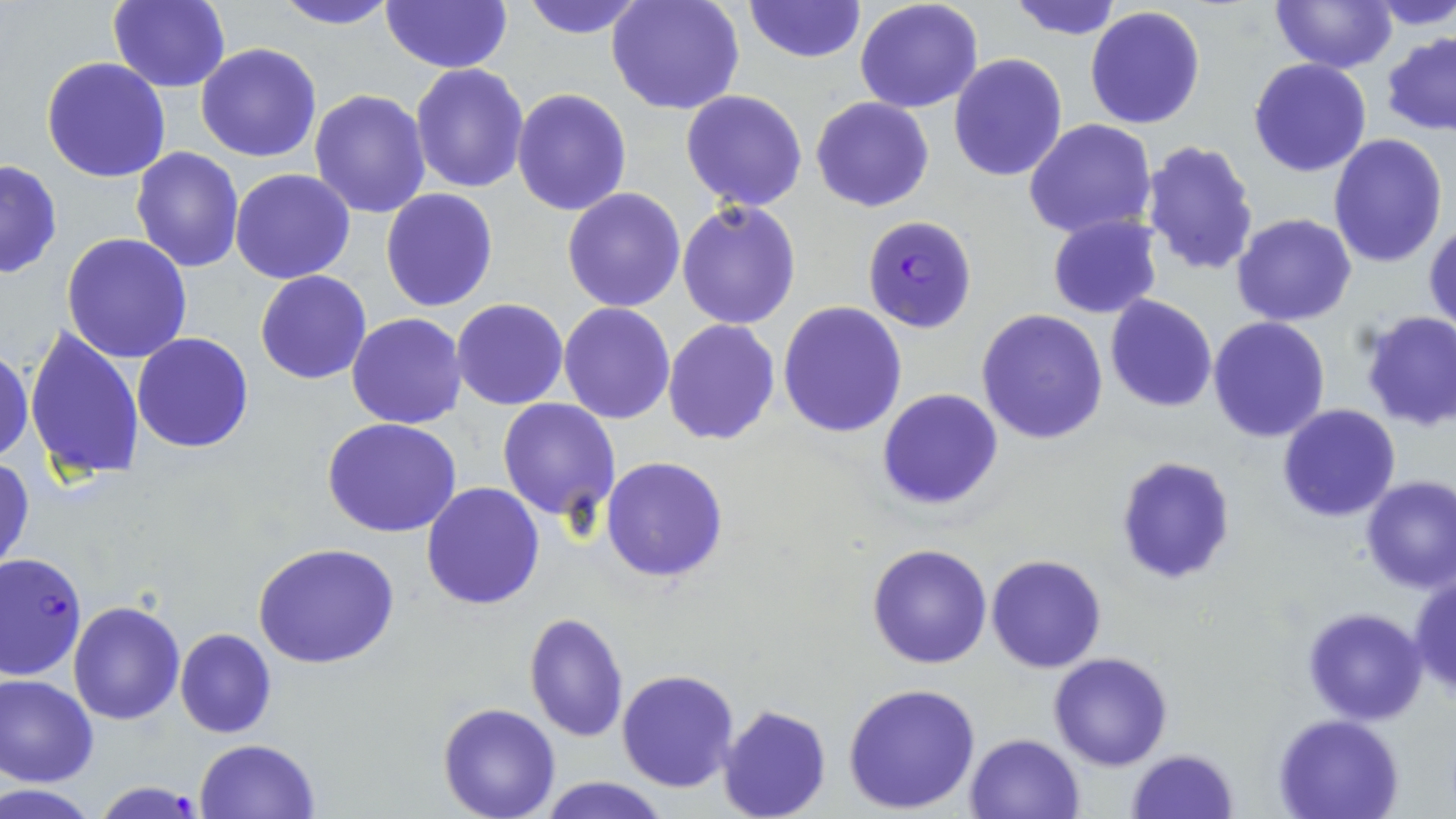

Summary:
  - Coordinate format: approximate bounding boxes as (x1, y1, x2, y2) in pixels
  - Plasmodium falciparum-infected red blood cell locations: (862, 214, 977, 332), (0, 552, 87, 683), (90, 779, 208, 818)
  - Uninfected red blood cell locations: (108, 0, 230, 93), (268, 0, 402, 30), (520, 0, 648, 39), (606, 0, 746, 117), (744, 0, 865, 64), (1005, 0, 1125, 41), (1269, 0, 1397, 72), (1370, 0, 1456, 30), (381, 1, 512, 74), (854, 1, 984, 113), (1085, 6, 1208, 130), (1382, 31, 1456, 137), (194, 43, 322, 163), (948, 53, 1068, 182), (41, 57, 172, 183), (1249, 57, 1372, 177), (409, 62, 529, 194), (310, 88, 433, 218), (513, 88, 632, 215), (680, 89, 809, 211), (811, 95, 936, 212), (1024, 118, 1159, 240), (1328, 132, 1448, 268), (1140, 139, 1260, 277), (131, 147, 246, 273), (0, 157, 62, 281), (229, 167, 357, 284), (381, 188, 498, 313), (562, 188, 685, 313), (676, 199, 802, 330), (1046, 213, 1163, 318), (1232, 213, 1357, 326), (1424, 218, 1456, 337), (61, 232, 192, 363), (255, 269, 372, 384), (1105, 294, 1217, 412), (452, 298, 568, 411), (777, 301, 907, 436), (558, 302, 675, 424), (976, 309, 1108, 446), (1358, 309, 1456, 431), (347, 313, 468, 428), (1207, 316, 1330, 443), (662, 320, 780, 445), (24, 325, 144, 483), (131, 332, 254, 453), (0, 340, 34, 466), (877, 388, 1003, 512), (497, 398, 619, 522), (1277, 404, 1401, 522), (322, 418, 462, 537), (1114, 453, 1239, 586), (0, 454, 35, 580), (601, 456, 729, 583), (1361, 475, 1456, 592), (421, 482, 545, 610), (867, 542, 994, 668), (254, 543, 402, 669), (987, 554, 1108, 673), (1409, 572, 1456, 701), (67, 602, 184, 725), (1303, 605, 1429, 724), (524, 613, 629, 741), (174, 627, 275, 738), (1048, 652, 1174, 771), (617, 669, 741, 792), (0, 675, 98, 787), (843, 682, 983, 815), (437, 701, 562, 819), (718, 703, 832, 819), (1273, 714, 1403, 818), (965, 733, 1086, 819), (195, 738, 321, 819), (1125, 748, 1239, 819), (535, 776, 672, 819)
  - Slide-level diagnosis: Plasmodium falciparum
  - Image size: 1456×819 pixels
  - Modality: light microscopy
  - Preparation: thin blood smear
  - Stain: May-Grünwald-Giemsa
  - Magnification: 1000x
  - Field of view: one of a larger specimen